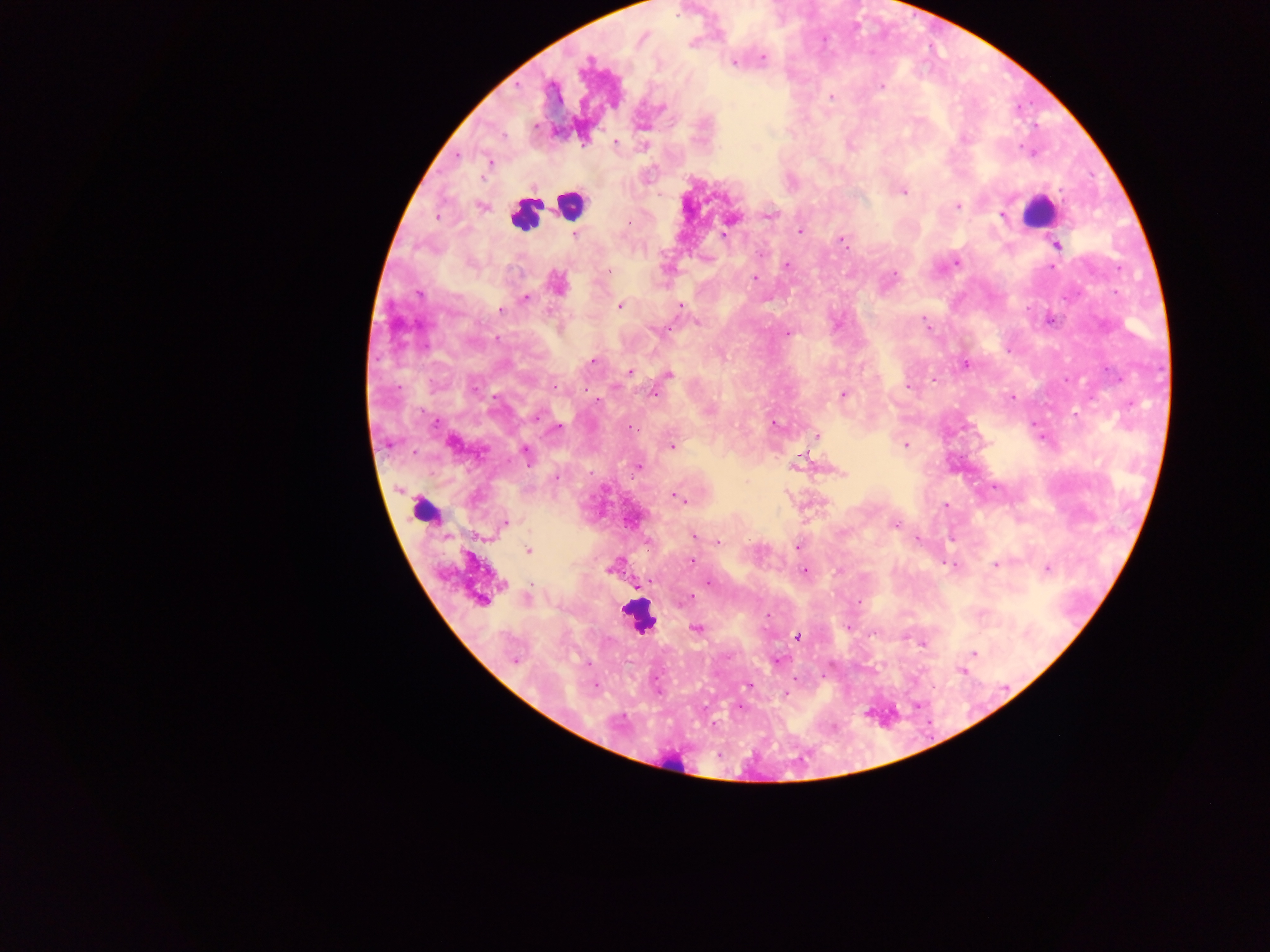

Approximate centers as (x, y) in pixels.
Summary:
  - Malaria parasite locations: (762, 57), (733, 61), (881, 86), (832, 96), (535, 126), (965, 138), (615, 142), (489, 163), (904, 191), (957, 206), (481, 207), (770, 215), (1001, 215), (437, 217), (628, 223), (800, 231), (724, 235), (575, 236), (842, 240), (1056, 244), (760, 254), (956, 263), (786, 265), (1053, 268), (609, 271), (894, 275), (755, 279), (557, 283), (418, 294), (525, 298), (680, 306), (619, 307), (500, 309), (924, 321), (697, 322), (788, 334), (592, 361), (965, 364), (629, 372), (670, 373), (555, 386), (907, 386), (475, 388), (653, 395), (843, 395), (1012, 398), (596, 400), (537, 416), (434, 422), (775, 423), (633, 428), (558, 429), (816, 436), (452, 443), (905, 445), (672, 446), (526, 454), (638, 467), (841, 473), (556, 477), (676, 497), (946, 505), (506, 523), (895, 524), (693, 537), (918, 539), (718, 541), (796, 546), (528, 551), (692, 561), (995, 564), (952, 566), (610, 568), (1047, 568), (804, 571), (708, 583), (504, 584), (640, 585), (528, 598), (688, 599), (481, 601), (768, 616), (697, 627), (797, 637), (922, 644), (974, 652), (515, 661), (777, 661), (961, 671), (747, 686), (785, 693)
  - Leukocyte locations (subset; some below the resolvable size): (570, 204), (1035, 210), (525, 216), (426, 508), (639, 618), (667, 762)
  - Preparation: thick blood smear
  - Image size: 1270×952 pixels
  - Country: Ghana
  - Field of view: single
  - Capture: mobile-phone photograph through a microscope